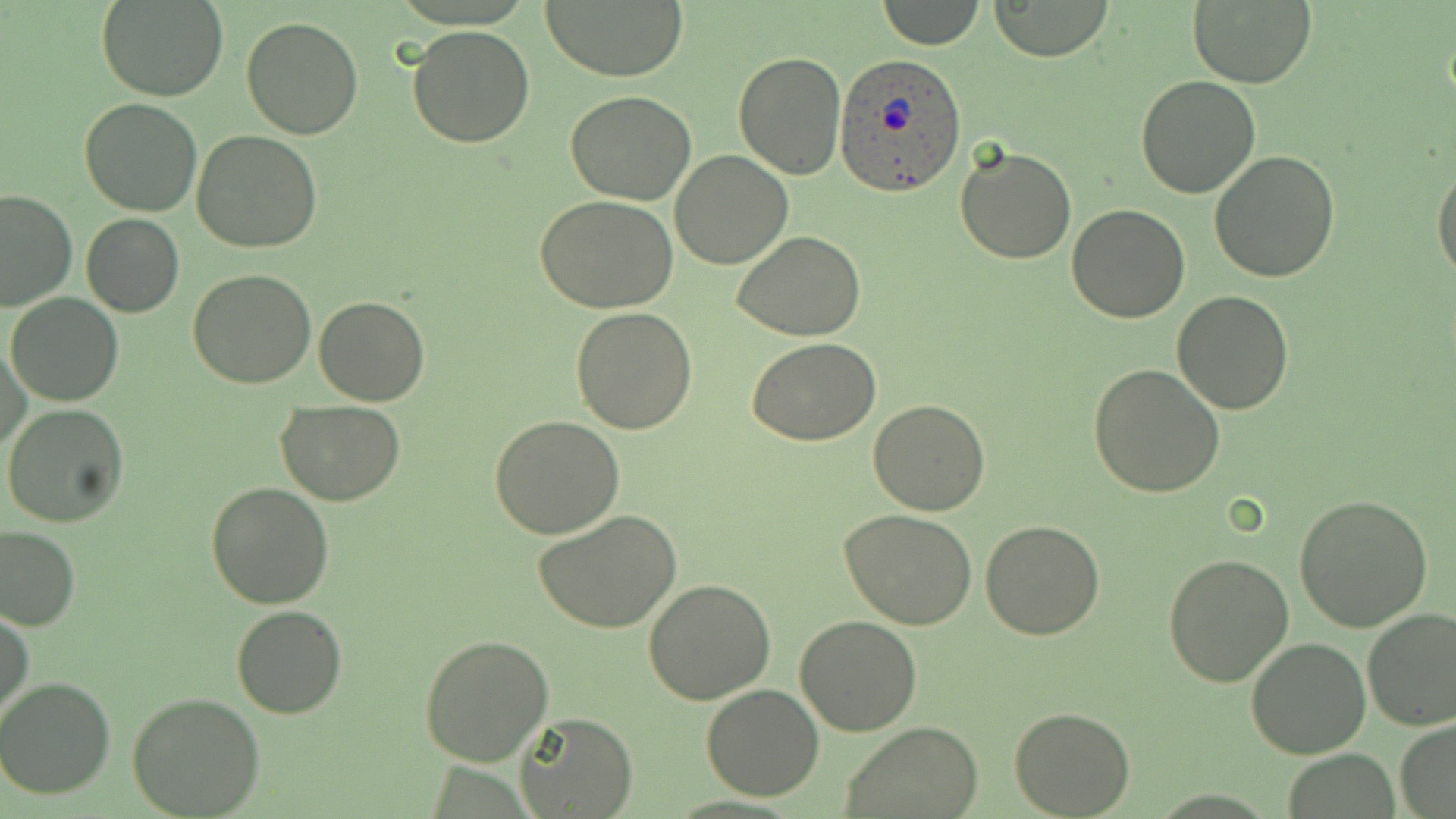

Summary:
  - Coordinate format: approximate bounding boxes as named x1/y1/x2/y2 corners in pixels
  - Plasmodium ovale-infected red blood cell locations: (x1=834, y1=55, x2=967, y2=195)
  - Uninfected red blood cell locations: (x1=539, y1=0, x2=690, y2=81), (x1=879, y1=0, x2=984, y2=49), (x1=98, y1=1, x2=227, y2=102), (x1=987, y1=1, x2=1113, y2=62), (x1=1188, y1=1, x2=1317, y2=87), (x1=240, y1=15, x2=364, y2=139), (x1=406, y1=25, x2=535, y2=149), (x1=733, y1=51, x2=847, y2=179), (x1=1134, y1=75, x2=1261, y2=198), (x1=565, y1=93, x2=695, y2=205), (x1=78, y1=98, x2=204, y2=218), (x1=192, y1=129, x2=323, y2=253), (x1=953, y1=144, x2=1075, y2=264), (x1=670, y1=150, x2=794, y2=269), (x1=1208, y1=151, x2=1341, y2=283), (x1=1432, y1=162, x2=1456, y2=282), (x1=0, y1=187, x2=77, y2=311), (x1=536, y1=198, x2=680, y2=314), (x1=1068, y1=203, x2=1189, y2=322), (x1=81, y1=213, x2=184, y2=318), (x1=732, y1=231, x2=866, y2=340), (x1=187, y1=270, x2=316, y2=389), (x1=1171, y1=289, x2=1294, y2=413), (x1=8, y1=293, x2=123, y2=405), (x1=313, y1=295, x2=430, y2=406), (x1=569, y1=307, x2=697, y2=432), (x1=749, y1=338, x2=880, y2=445), (x1=2, y1=339, x2=29, y2=454), (x1=1088, y1=365, x2=1225, y2=500), (x1=277, y1=399, x2=404, y2=506), (x1=868, y1=399, x2=992, y2=516), (x1=3, y1=404, x2=129, y2=528), (x1=491, y1=414, x2=624, y2=539), (x1=205, y1=483, x2=334, y2=609), (x1=1293, y1=494, x2=1433, y2=632), (x1=534, y1=508, x2=683, y2=634), (x1=838, y1=509, x2=980, y2=630), (x1=980, y1=520, x2=1106, y2=639), (x1=0, y1=527, x2=81, y2=630), (x1=1162, y1=554, x2=1296, y2=687), (x1=644, y1=578, x2=776, y2=703), (x1=230, y1=605, x2=348, y2=719), (x1=0, y1=607, x2=33, y2=728), (x1=1362, y1=608, x2=1456, y2=732), (x1=795, y1=615, x2=923, y2=735), (x1=420, y1=633, x2=554, y2=766), (x1=1243, y1=637, x2=1370, y2=758), (x1=0, y1=678, x2=115, y2=800), (x1=700, y1=685, x2=826, y2=801), (x1=127, y1=691, x2=265, y2=817), (x1=1010, y1=707, x2=1136, y2=818), (x1=514, y1=711, x2=638, y2=819), (x1=1394, y1=717, x2=1456, y2=818), (x1=840, y1=721, x2=985, y2=819), (x1=1282, y1=748, x2=1401, y2=819)
  - Slide-level diagnosis: Plasmodium ovale
  - Preparation: thin blood smear
  - Image size: 1456×819 pixels
  - Field of view: single
  - Magnification: 1000x
  - Modality: optical microscopy
  - Stain: May-Grünwald-Giemsa